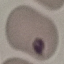
result: no malaria parasites detected
image_type: cell patch, automatically extracted from a larger field of view and resized to 64 × 64 pixels
capture: smartphone through the microscope eyepiece
stain: Giemsa
preparation: thin blood film